Assess this cell for malaria.
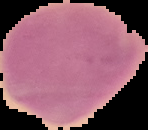
It is parasitized.

Summary:
  - Image type: cell region segmented out of the field of view; surrounding area masked to black
  - Preparation: thin blood smear
  - Image size: 148×130 pixels